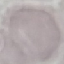
Summary:
  - Malaria status: uninfected
  - Stain: Giemsa
  - Image type: automatically extracted cell patch, resized to 64 × 64 pixels
  - Preparation: thin blood smear
  - Capture: smartphone through the microscope eyepiece